Locate platelets.
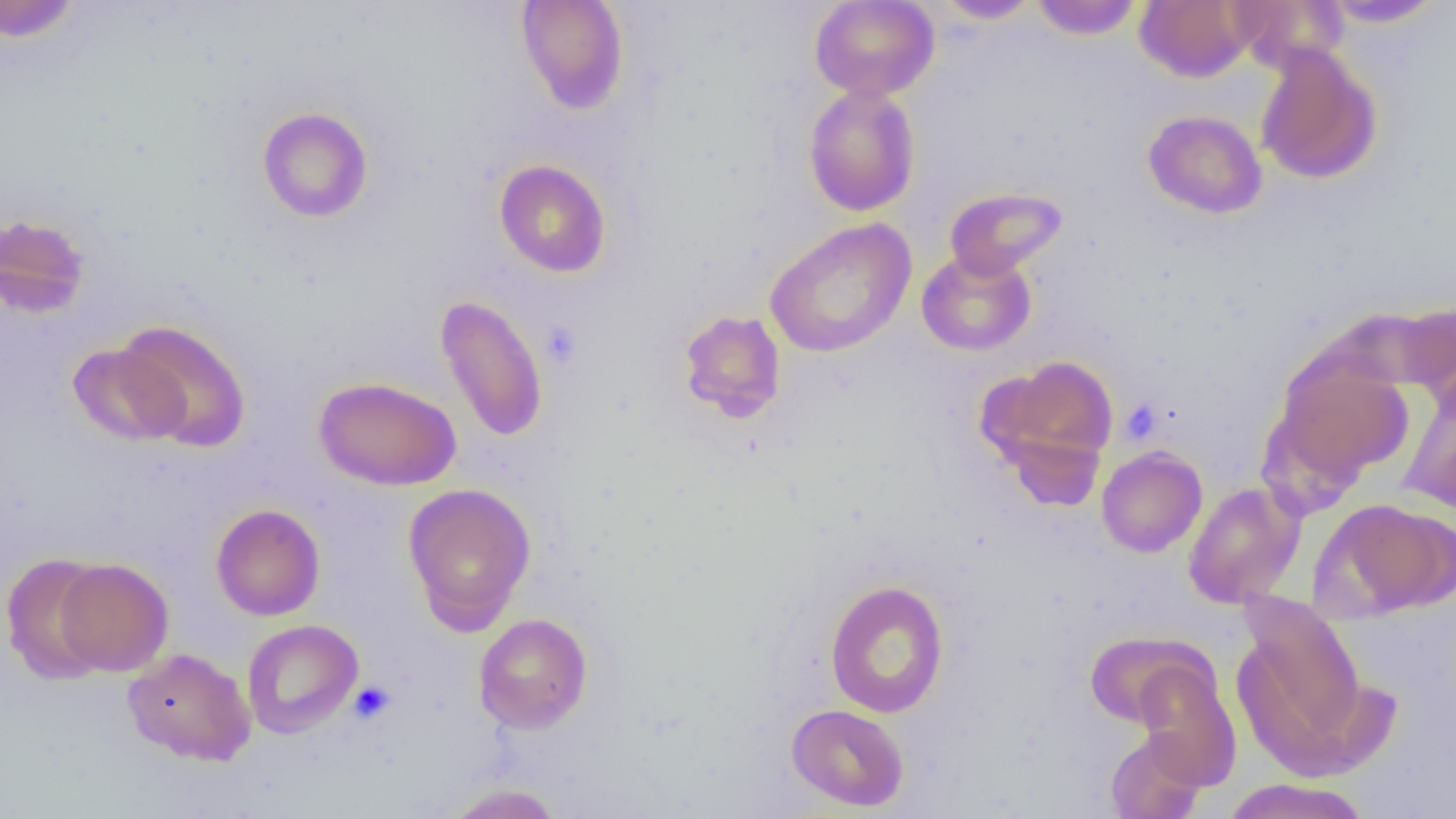
Approximate bounding boxes as named x1/y1/x2/y2 corners in pixels.
Platelets: (x1=541, y1=321, x2=583, y2=368), (x1=1121, y1=400, x2=1162, y2=444), (x1=349, y1=681, x2=396, y2=724).

Uninfected red blood cell locations: (x1=0, y1=0, x2=83, y2=42), (x1=515, y1=0, x2=630, y2=115), (x1=809, y1=0, x2=939, y2=101), (x1=934, y1=0, x2=1042, y2=23), (x1=1030, y1=0, x2=1144, y2=40), (x1=1135, y1=0, x2=1255, y2=82), (x1=1227, y1=0, x2=1349, y2=73), (x1=1320, y1=0, x2=1446, y2=28), (x1=1254, y1=44, x2=1382, y2=185), (x1=803, y1=83, x2=921, y2=217), (x1=257, y1=107, x2=374, y2=223), (x1=1143, y1=109, x2=1268, y2=218), (x1=494, y1=159, x2=612, y2=278), (x1=943, y1=186, x2=1068, y2=281), (x1=0, y1=213, x2=91, y2=319), (x1=764, y1=217, x2=917, y2=358), (x1=916, y1=249, x2=1036, y2=356), (x1=435, y1=295, x2=549, y2=443), (x1=1395, y1=302, x2=1456, y2=410), (x1=676, y1=309, x2=787, y2=423), (x1=115, y1=318, x2=251, y2=451), (x1=67, y1=342, x2=189, y2=446), (x1=1272, y1=353, x2=1414, y2=487), (x1=980, y1=354, x2=1120, y2=486), (x1=314, y1=376, x2=462, y2=490), (x1=1398, y1=387, x2=1456, y2=512), (x1=1096, y1=446, x2=1207, y2=558), (x1=1183, y1=482, x2=1304, y2=608), (x1=403, y1=483, x2=537, y2=633), (x1=1316, y1=498, x2=1456, y2=620), (x1=211, y1=503, x2=325, y2=621), (x1=1, y1=554, x2=113, y2=685), (x1=54, y1=558, x2=173, y2=676), (x1=824, y1=580, x2=949, y2=718), (x1=1235, y1=589, x2=1368, y2=762), (x1=473, y1=613, x2=593, y2=733), (x1=242, y1=618, x2=363, y2=738), (x1=1084, y1=631, x2=1209, y2=728), (x1=122, y1=648, x2=256, y2=765), (x1=1133, y1=661, x2=1241, y2=789), (x1=786, y1=704, x2=909, y2=811), (x1=1106, y1=731, x2=1206, y2=819), (x1=1221, y1=778, x2=1370, y2=819), (x1=442, y1=783, x2=564, y2=819). Slide-level diagnosis: negative for blood parasites. Thin blood film. One field of a larger specimen. Optical microscopy. Image is 1456×819 pixels. 1000x magnification.